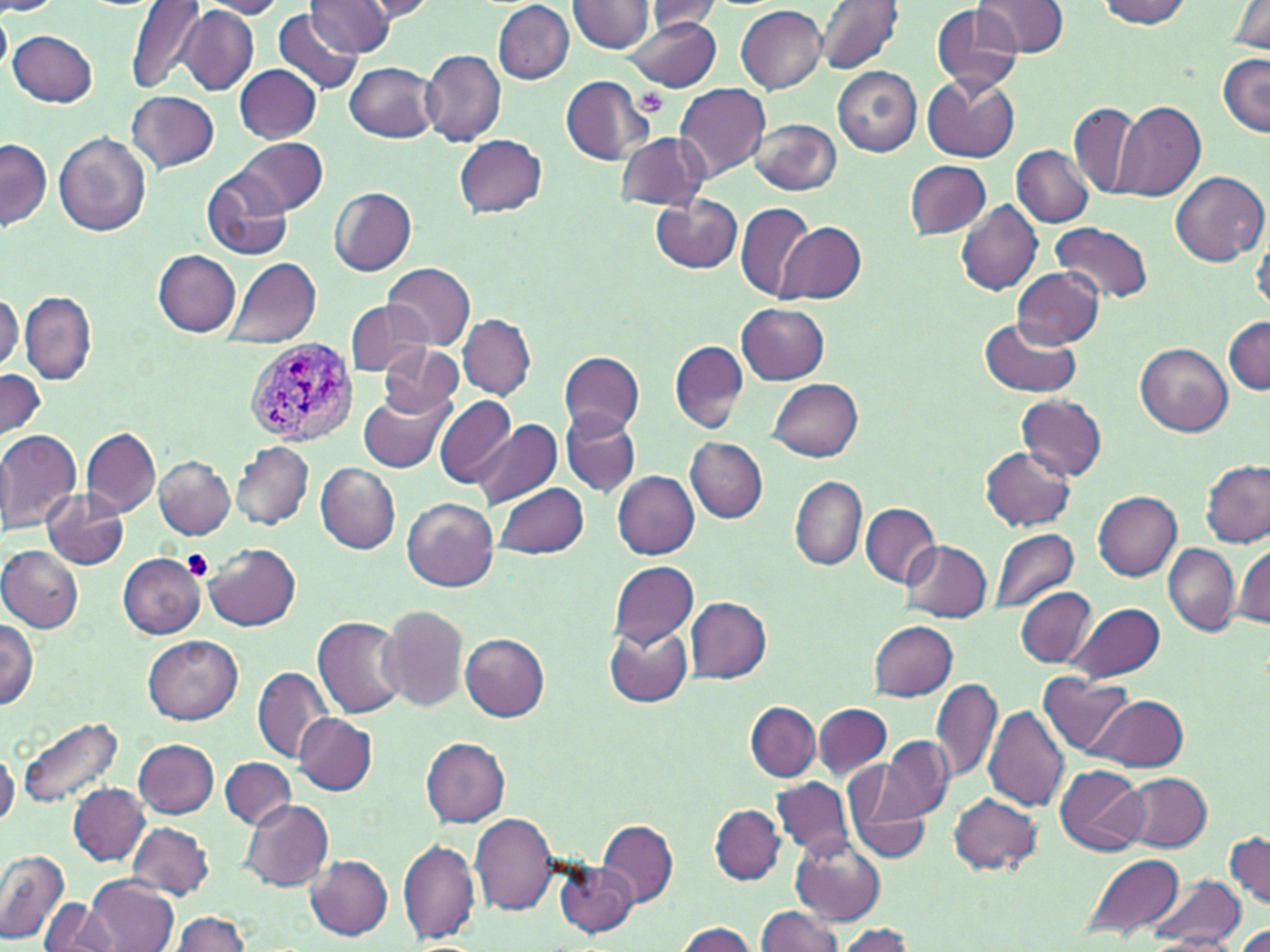

slide-level diagnosis = Plasmodium vivax
platelet locations = approximate bounding boxes as named x1/y1/x2/y2 corners in pixels: (x1=637, y1=88, x2=670, y2=116), (x1=182, y1=549, x2=213, y2=580)
modality = light microscopy
field of view = one of a larger specimen
magnification = 1000x
stain = May-Grünwald-Giemsa
Plasmodium vivax-infected red blood cell locations = approximate bounding boxes as named x1/y1/x2/y2 corners in pixels: (x1=245, y1=338, x2=358, y2=447)
uninfected red blood cell locations = approximate bounding boxes as named x1/y1/x2/y2 corners in pixels: (x1=193, y1=0, x2=288, y2=18), (x1=355, y1=0, x2=438, y2=21), (x1=814, y1=0, x2=903, y2=75), (x1=975, y1=0, x2=1069, y2=58), (x1=0, y1=1, x2=62, y2=16), (x1=125, y1=1, x2=209, y2=95), (x1=305, y1=1, x2=395, y2=56), (x1=567, y1=1, x2=655, y2=53), (x1=493, y1=2, x2=575, y2=84), (x1=639, y1=2, x2=725, y2=36), (x1=1095, y1=2, x2=1195, y2=27), (x1=1228, y1=3, x2=1270, y2=54), (x1=932, y1=5, x2=1024, y2=93), (x1=737, y1=6, x2=826, y2=93), (x1=0, y1=8, x2=11, y2=78), (x1=176, y1=9, x2=258, y2=96), (x1=272, y1=9, x2=363, y2=98), (x1=625, y1=14, x2=721, y2=93), (x1=8, y1=29, x2=97, y2=107), (x1=421, y1=49, x2=506, y2=144), (x1=1218, y1=52, x2=1269, y2=136), (x1=345, y1=61, x2=439, y2=142), (x1=235, y1=65, x2=322, y2=143), (x1=833, y1=68, x2=921, y2=156), (x1=923, y1=74, x2=1019, y2=161), (x1=561, y1=75, x2=655, y2=165), (x1=675, y1=83, x2=771, y2=181), (x1=127, y1=91, x2=219, y2=172), (x1=1069, y1=101, x2=1144, y2=201), (x1=1113, y1=101, x2=1205, y2=201), (x1=752, y1=120, x2=841, y2=193), (x1=55, y1=131, x2=151, y2=236), (x1=616, y1=131, x2=710, y2=211), (x1=456, y1=134, x2=546, y2=216), (x1=1, y1=138, x2=52, y2=230), (x1=235, y1=138, x2=327, y2=216), (x1=1012, y1=145, x2=1093, y2=227), (x1=906, y1=160, x2=991, y2=239), (x1=1170, y1=170, x2=1267, y2=264), (x1=201, y1=171, x2=293, y2=260), (x1=329, y1=187, x2=416, y2=274), (x1=649, y1=193, x2=740, y2=273), (x1=955, y1=199, x2=1041, y2=296), (x1=735, y1=202, x2=814, y2=299), (x1=777, y1=220, x2=866, y2=303), (x1=1054, y1=222, x2=1153, y2=303), (x1=1251, y1=231, x2=1270, y2=315), (x1=153, y1=250, x2=242, y2=336), (x1=223, y1=257, x2=321, y2=349), (x1=381, y1=262, x2=474, y2=349), (x1=1011, y1=266, x2=1105, y2=346), (x1=19, y1=292, x2=97, y2=385), (x1=1, y1=294, x2=23, y2=373), (x1=345, y1=299, x2=429, y2=378), (x1=737, y1=303, x2=829, y2=385), (x1=459, y1=313, x2=534, y2=399), (x1=1225, y1=316, x2=1270, y2=394), (x1=980, y1=317, x2=1080, y2=397), (x1=669, y1=340, x2=749, y2=433), (x1=376, y1=344, x2=465, y2=416), (x1=1136, y1=344, x2=1231, y2=436), (x1=560, y1=350, x2=644, y2=435), (x1=0, y1=369, x2=46, y2=445), (x1=769, y1=378, x2=862, y2=461), (x1=358, y1=384, x2=455, y2=472), (x1=1016, y1=394, x2=1106, y2=481), (x1=434, y1=395, x2=516, y2=488), (x1=560, y1=408, x2=640, y2=497), (x1=473, y1=419, x2=561, y2=510), (x1=82, y1=427, x2=160, y2=516), (x1=0, y1=429, x2=83, y2=535), (x1=686, y1=438, x2=767, y2=523), (x1=0, y1=440, x2=14, y2=531), (x1=231, y1=442, x2=313, y2=529), (x1=979, y1=446, x2=1075, y2=530), (x1=154, y1=455, x2=235, y2=539), (x1=1200, y1=459, x2=1269, y2=547), (x1=315, y1=464, x2=400, y2=554), (x1=614, y1=470, x2=699, y2=560), (x1=790, y1=476, x2=866, y2=570), (x1=496, y1=482, x2=590, y2=559), (x1=44, y1=488, x2=129, y2=568), (x1=1093, y1=492, x2=1181, y2=580), (x1=403, y1=498, x2=498, y2=591), (x1=861, y1=503, x2=940, y2=588), (x1=990, y1=528, x2=1079, y2=615), (x1=902, y1=540, x2=991, y2=622), (x1=204, y1=542, x2=301, y2=630), (x1=1163, y1=543, x2=1240, y2=636), (x1=1232, y1=544, x2=1270, y2=630), (x1=0, y1=546, x2=83, y2=632), (x1=119, y1=553, x2=206, y2=639), (x1=609, y1=561, x2=699, y2=648), (x1=1016, y1=587, x2=1096, y2=668), (x1=686, y1=597, x2=771, y2=683), (x1=1069, y1=602, x2=1165, y2=683), (x1=378, y1=603, x2=468, y2=711), (x1=313, y1=616, x2=407, y2=719), (x1=0, y1=617, x2=37, y2=708), (x1=870, y1=622, x2=958, y2=700), (x1=605, y1=625, x2=691, y2=706), (x1=460, y1=633, x2=550, y2=721), (x1=144, y1=634, x2=244, y2=723), (x1=253, y1=667, x2=331, y2=763), (x1=1040, y1=675, x2=1133, y2=757), (x1=931, y1=676, x2=1002, y2=786), (x1=1092, y1=694, x2=1188, y2=771), (x1=747, y1=702, x2=820, y2=781), (x1=815, y1=703, x2=891, y2=780), (x1=983, y1=703, x2=1070, y2=811), (x1=296, y1=713, x2=376, y2=795), (x1=17, y1=716, x2=125, y2=811), (x1=879, y1=735, x2=953, y2=822), (x1=422, y1=738, x2=509, y2=827), (x1=135, y1=739, x2=218, y2=818), (x1=0, y1=747, x2=17, y2=829), (x1=220, y1=757, x2=294, y2=831), (x1=842, y1=763, x2=931, y2=866), (x1=1055, y1=764, x2=1149, y2=856), (x1=1122, y1=772, x2=1211, y2=852), (x1=773, y1=777, x2=853, y2=857), (x1=67, y1=783, x2=151, y2=866), (x1=949, y1=793, x2=1042, y2=875), (x1=240, y1=800, x2=333, y2=893), (x1=711, y1=805, x2=783, y2=884), (x1=470, y1=813, x2=560, y2=916), (x1=598, y1=819, x2=677, y2=908), (x1=127, y1=822, x2=214, y2=900), (x1=1225, y1=833, x2=1270, y2=908), (x1=790, y1=834, x2=885, y2=925), (x1=398, y1=838, x2=479, y2=945), (x1=0, y1=849, x2=70, y2=944), (x1=1083, y1=853, x2=1185, y2=939), (x1=304, y1=855, x2=392, y2=939), (x1=554, y1=859, x2=637, y2=937), (x1=87, y1=874, x2=178, y2=952), (x1=1148, y1=876, x2=1243, y2=948), (x1=42, y1=900, x2=112, y2=951), (x1=756, y1=906, x2=844, y2=952), (x1=171, y1=912, x2=253, y2=951), (x1=672, y1=922, x2=758, y2=952), (x1=1149, y1=922, x2=1246, y2=951), (x1=1233, y1=923, x2=1270, y2=951), (x1=835, y1=925, x2=912, y2=952)
preparation = thin blood smear
image size = 1270×952 pixels